Outline each blood parasite and name the species.
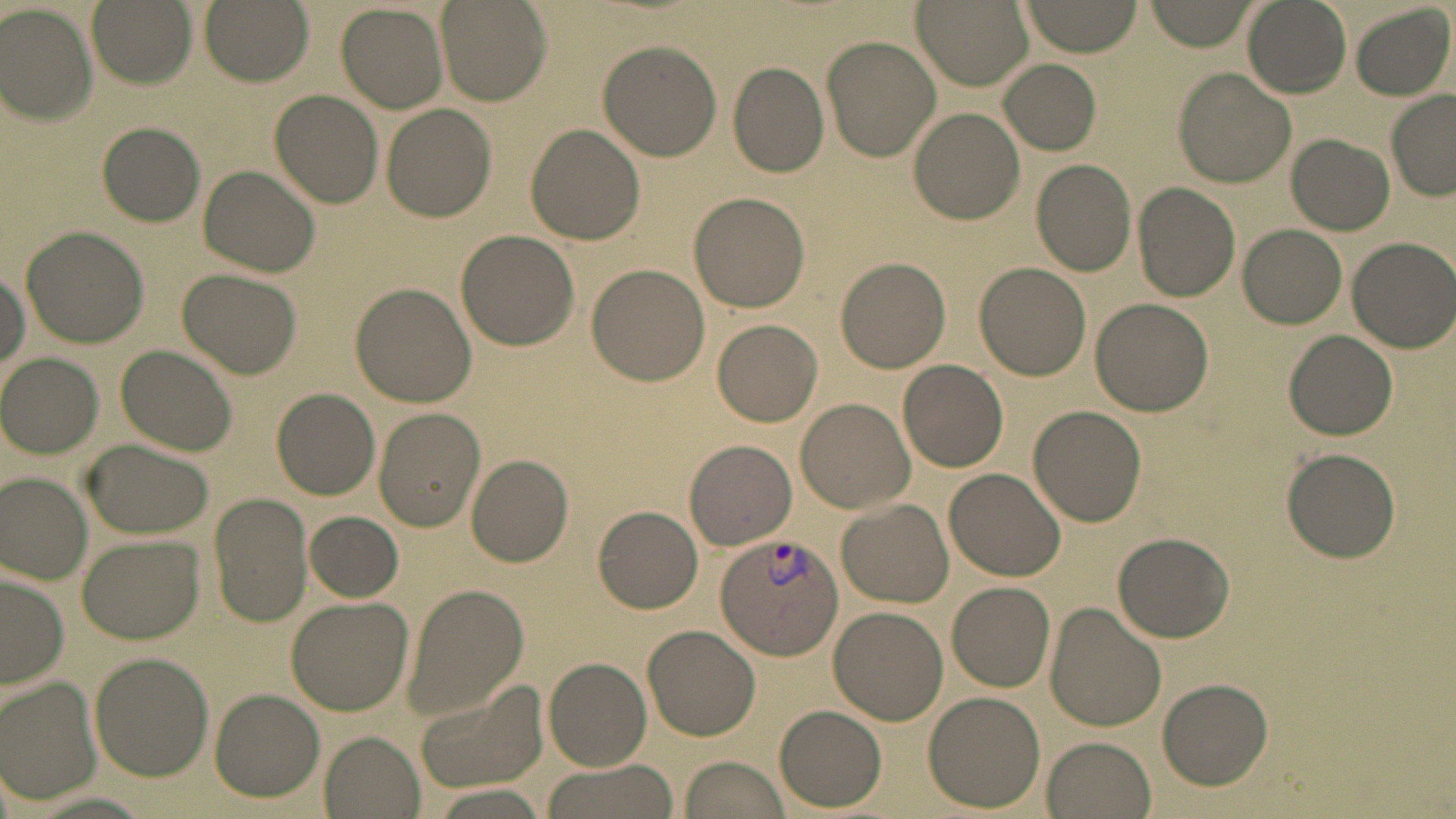

Approximate bounding boxes as named x1/y1/x2/y2 corners in pixels.
Plasmodium vivax-infected red blood cells: (x1=715, y1=534, x2=844, y2=659).
No Plasmodium falciparum, Plasmodium ovale, Plasmodium malariae, Babesia divergens, or Trypanosoma brucei observed.

Summary:
  - Uninfected red blood cell locations: (x1=86, y1=0, x2=196, y2=87), (x1=200, y1=0, x2=313, y2=84), (x1=911, y1=0, x2=1032, y2=91), (x1=1021, y1=0, x2=1143, y2=56), (x1=1145, y1=0, x2=1258, y2=51), (x1=1242, y1=0, x2=1352, y2=97), (x1=437, y1=1, x2=551, y2=106), (x1=338, y1=3, x2=449, y2=113), (x1=1351, y1=3, x2=1455, y2=101), (x1=0, y1=4, x2=98, y2=122), (x1=823, y1=33, x2=942, y2=162), (x1=597, y1=40, x2=722, y2=161), (x1=998, y1=59, x2=1101, y2=154), (x1=727, y1=62, x2=829, y2=178), (x1=1174, y1=69, x2=1295, y2=186), (x1=269, y1=90, x2=383, y2=209), (x1=1386, y1=94, x2=1456, y2=200), (x1=381, y1=105, x2=497, y2=222), (x1=908, y1=107, x2=1026, y2=224), (x1=96, y1=122, x2=205, y2=226), (x1=526, y1=123, x2=646, y2=245), (x1=1288, y1=134, x2=1393, y2=234), (x1=1030, y1=161, x2=1136, y2=276), (x1=198, y1=164, x2=320, y2=279), (x1=1134, y1=182, x2=1243, y2=301), (x1=688, y1=190, x2=812, y2=313), (x1=1238, y1=224, x2=1346, y2=329), (x1=21, y1=226, x2=149, y2=348), (x1=455, y1=229, x2=579, y2=351), (x1=1347, y1=237, x2=1456, y2=353), (x1=835, y1=256, x2=950, y2=372), (x1=975, y1=262, x2=1093, y2=380), (x1=586, y1=264, x2=710, y2=387), (x1=1, y1=267, x2=30, y2=379), (x1=177, y1=268, x2=301, y2=378), (x1=350, y1=283, x2=475, y2=407), (x1=1092, y1=299, x2=1215, y2=417), (x1=710, y1=318, x2=823, y2=427), (x1=1286, y1=330, x2=1397, y2=438), (x1=116, y1=344, x2=237, y2=456), (x1=1, y1=353, x2=102, y2=458), (x1=898, y1=360, x2=1009, y2=472), (x1=270, y1=388, x2=382, y2=499), (x1=794, y1=399, x2=914, y2=514), (x1=1028, y1=406, x2=1146, y2=526), (x1=372, y1=408, x2=484, y2=531), (x1=685, y1=439, x2=797, y2=550), (x1=80, y1=440, x2=213, y2=538), (x1=1282, y1=448, x2=1399, y2=563), (x1=464, y1=454, x2=574, y2=567), (x1=946, y1=468, x2=1066, y2=581), (x1=1, y1=473, x2=94, y2=584), (x1=208, y1=494, x2=312, y2=627), (x1=837, y1=499, x2=954, y2=607), (x1=594, y1=505, x2=703, y2=613), (x1=304, y1=511, x2=403, y2=603), (x1=1111, y1=531, x2=1236, y2=643), (x1=76, y1=535, x2=206, y2=644), (x1=1, y1=572, x2=68, y2=691), (x1=948, y1=580, x2=1057, y2=692), (x1=400, y1=584, x2=529, y2=722), (x1=285, y1=597, x2=414, y2=715), (x1=1045, y1=603, x2=1166, y2=734), (x1=828, y1=606, x2=948, y2=725), (x1=642, y1=624, x2=762, y2=742), (x1=89, y1=652, x2=214, y2=780), (x1=543, y1=657, x2=650, y2=769), (x1=2, y1=677, x2=103, y2=806), (x1=1156, y1=678, x2=1274, y2=790), (x1=411, y1=682, x2=549, y2=795), (x1=209, y1=690, x2=323, y2=801), (x1=921, y1=691, x2=1046, y2=811), (x1=775, y1=706, x2=887, y2=811), (x1=317, y1=732, x2=423, y2=818), (x1=1041, y1=736, x2=1155, y2=819), (x1=679, y1=755, x2=791, y2=819), (x1=537, y1=759, x2=678, y2=819), (x1=422, y1=783, x2=555, y2=819)
  - Slide-level diagnosis: Plasmodium vivax
  - Image size: 1456×819 pixels
  - Magnification: 1000x
  - Modality: light microscopy
  - Stain: May-Grünwald-Giemsa
  - Preparation: thin blood smear
  - Field of view: one of a larger specimen